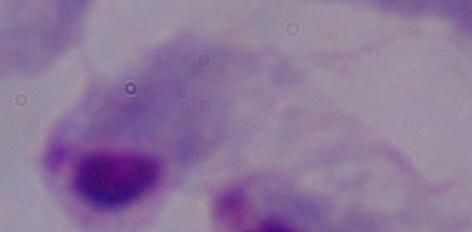

Captured at 1000x magnification. A trichomonad is shown. Photomicrograph.